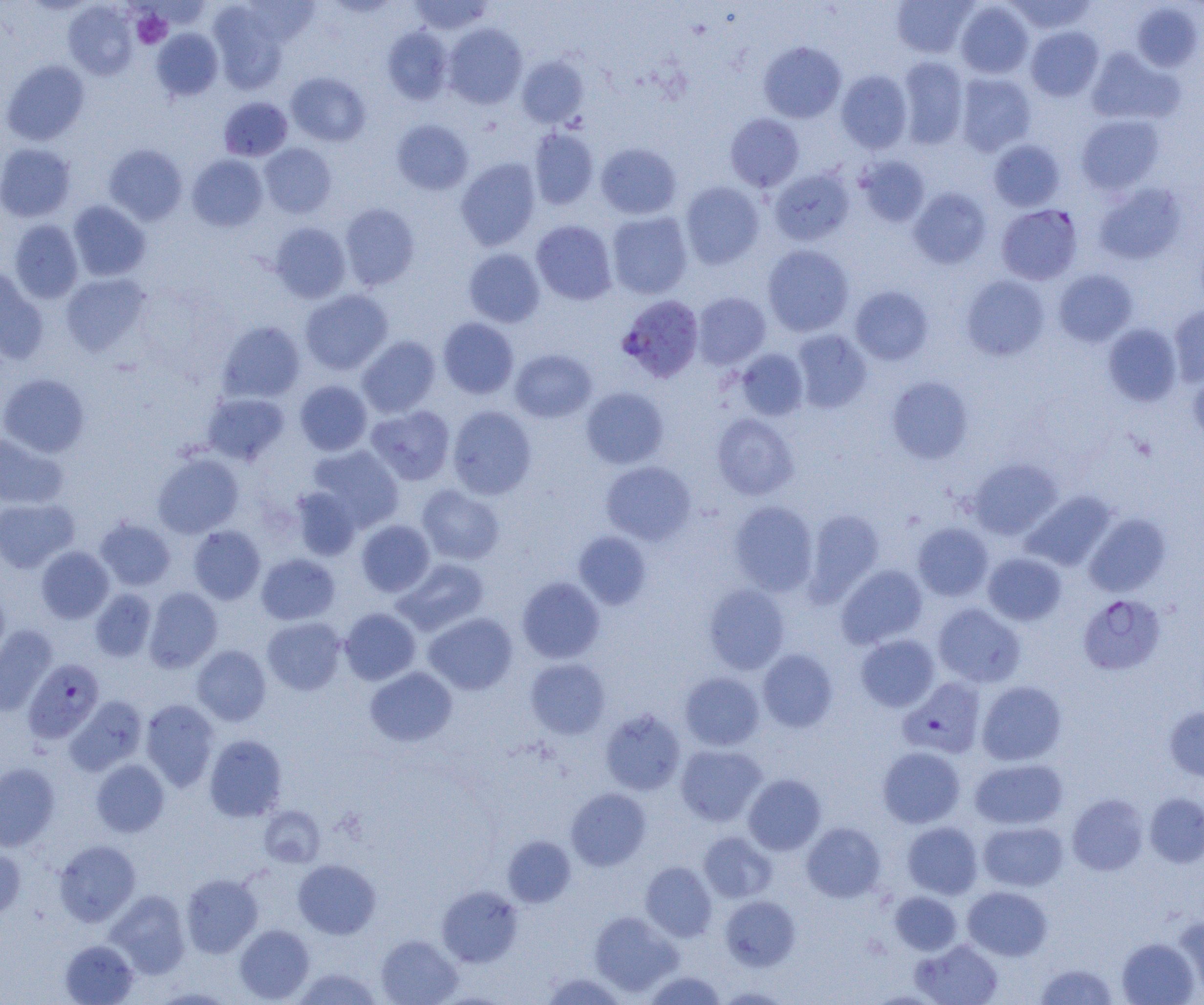
slide-level diagnosis = Plasmodium falciparum
magnification = 1000x
image size = 1204×1005 pixels
platelet locations = approximate bounding boxes as [x1, y1, x2, y2] in pixels: [131, 11, 171, 48]
field of view = one of a larger specimen
Plasmodium falciparum-infected red blood cell locations = approximate bounding boxes as [x1, y1, x2, y2] in pixels: [997, 204, 1082, 285], [617, 295, 704, 382], [1078, 594, 1166, 676], [23, 658, 104, 743], [899, 677, 986, 758]
preparation = thin blood smear
uninfected red blood cell locations = approximate bounding boxes as [x1, y1, x2, y2] in pixels: [408, 0, 494, 35], [891, 0, 977, 58], [241, 1, 320, 46], [955, 1, 1034, 79], [1004, 1, 1097, 34], [63, 2, 138, 80], [1131, 3, 1203, 71], [208, 5, 287, 94], [443, 23, 527, 109], [382, 26, 453, 105], [1025, 26, 1104, 101], [151, 28, 223, 101], [758, 41, 847, 123], [1086, 47, 1184, 125], [517, 56, 589, 128], [896, 56, 969, 149], [1, 60, 90, 145], [836, 70, 912, 153], [286, 72, 370, 147], [955, 72, 1037, 156], [218, 96, 292, 161], [725, 113, 804, 191], [1076, 115, 1165, 194], [392, 119, 473, 195], [528, 128, 599, 210], [988, 139, 1065, 211], [0, 143, 76, 222], [259, 143, 337, 218], [596, 143, 681, 219], [103, 144, 187, 225], [187, 154, 268, 232], [856, 156, 930, 227], [455, 158, 541, 250], [769, 168, 854, 246], [680, 181, 764, 269], [1093, 182, 1187, 265], [908, 187, 991, 268], [67, 201, 151, 281], [339, 203, 420, 290], [607, 212, 693, 299], [9, 220, 83, 303], [531, 220, 617, 305], [269, 222, 351, 303], [762, 245, 854, 336], [463, 248, 545, 327], [0, 266, 48, 365], [1053, 269, 1137, 347], [60, 272, 152, 356], [961, 275, 1050, 360], [849, 286, 933, 365], [300, 289, 393, 375], [692, 292, 771, 370], [1168, 304, 1204, 387], [438, 317, 518, 399], [217, 320, 306, 403], [1103, 323, 1183, 407], [790, 329, 871, 414], [357, 335, 441, 417], [735, 348, 809, 420], [510, 349, 596, 423], [1188, 368, 1204, 447], [0, 373, 90, 457], [887, 376, 973, 464], [295, 380, 372, 455], [581, 387, 669, 468], [202, 392, 290, 465], [365, 405, 455, 484], [447, 406, 536, 499], [712, 412, 799, 500], [0, 432, 69, 509], [307, 445, 404, 532], [152, 452, 244, 538], [968, 458, 1062, 540], [601, 461, 696, 545], [417, 485, 505, 565], [291, 487, 362, 560], [1022, 490, 1117, 571], [0, 498, 78, 572], [729, 501, 819, 596], [804, 509, 884, 604], [1084, 513, 1170, 596], [94, 517, 176, 591], [356, 519, 434, 596], [912, 522, 993, 601], [188, 525, 265, 604], [573, 531, 652, 610], [36, 546, 115, 623], [982, 552, 1066, 626], [256, 553, 340, 625], [394, 558, 489, 635], [836, 564, 928, 649], [517, 576, 605, 663], [703, 583, 790, 674], [144, 587, 222, 672], [90, 588, 156, 661], [0, 589, 10, 668], [933, 603, 1025, 688], [339, 608, 421, 684], [424, 612, 517, 694], [262, 617, 347, 695], [0, 625, 57, 716], [856, 634, 939, 712], [191, 645, 271, 726], [757, 649, 838, 732], [526, 658, 611, 739], [365, 666, 457, 747], [680, 672, 764, 750], [977, 680, 1066, 765], [65, 695, 147, 775], [140, 699, 219, 791], [1164, 706, 1204, 782], [600, 708, 686, 795], [204, 734, 287, 822], [675, 744, 766, 826], [877, 746, 965, 827], [970, 758, 1067, 830], [91, 759, 169, 837], [0, 763, 60, 851], [743, 773, 826, 855], [566, 787, 651, 870], [1144, 792, 1204, 868], [1067, 793, 1148, 875], [259, 806, 325, 867], [902, 821, 983, 899], [978, 821, 1068, 891], [802, 822, 886, 902], [699, 831, 776, 903], [502, 835, 576, 907], [54, 840, 141, 926], [0, 846, 26, 920], [293, 859, 381, 939], [640, 861, 717, 941], [181, 873, 263, 958], [963, 885, 1052, 961], [437, 886, 523, 967], [106, 890, 191, 978], [890, 892, 962, 955], [720, 895, 800, 971], [590, 911, 683, 997], [1173, 916, 1204, 998], [235, 924, 314, 1003], [376, 934, 462, 1005], [1117, 937, 1199, 1005], [60, 939, 139, 1005], [912, 939, 1004, 1005], [1034, 962, 1119, 1005], [292, 967, 383, 1004], [540, 971, 628, 1004], [643, 971, 727, 1004], [716, 987, 791, 1004], [150, 988, 238, 1004]
modality = light microscopy